Identify the preparation type.
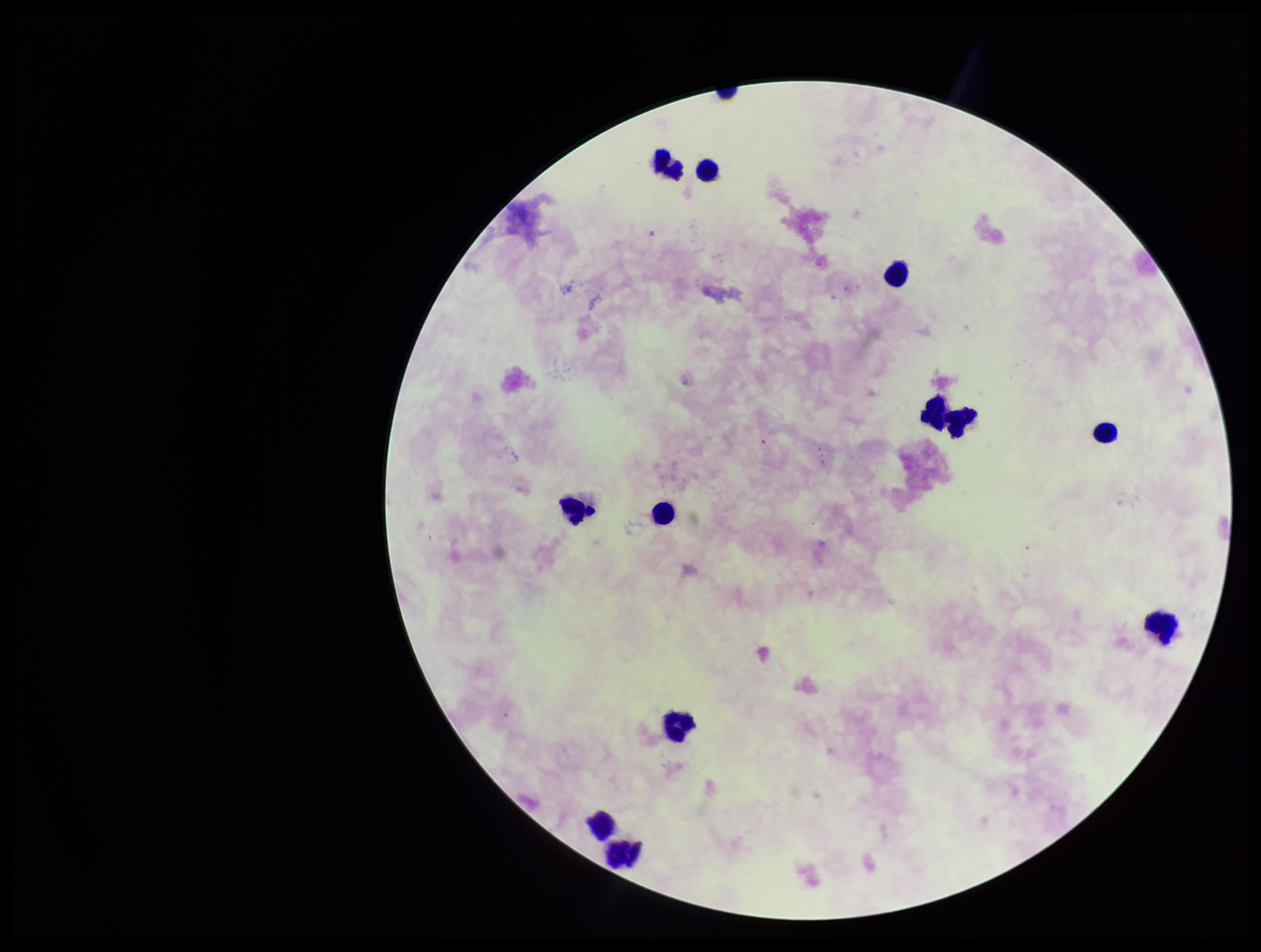
A thick smear.

patient malaria status = negative
capture = smartphone photograph through the microscope eyepiece
field of view = single
leukocyte count = 13
image size = 1261×952 pixels
stain = Giemsa
parasite count = 0
Plasmodium parasites = none identified